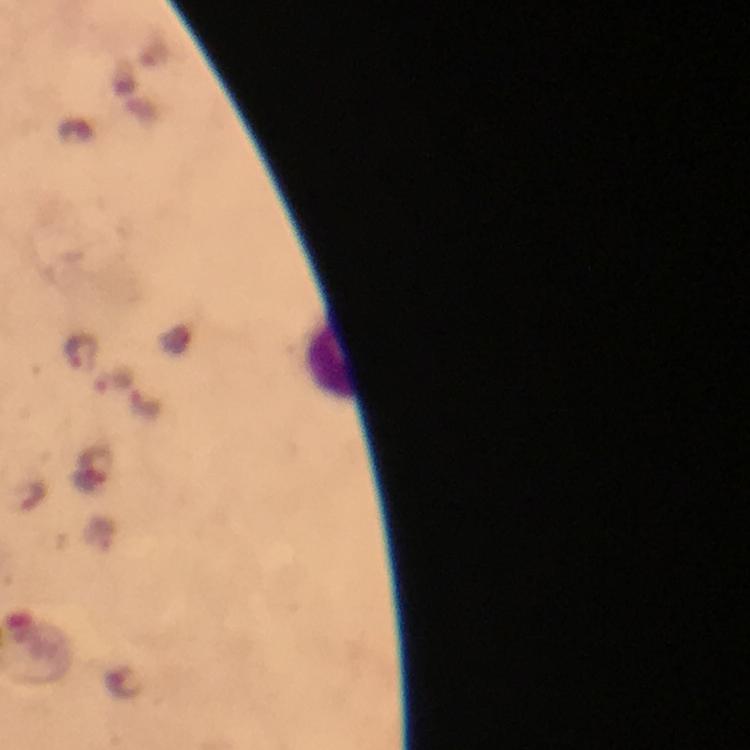

Approximate object centers, in pixels from the top-left corner. Malaria parasite locations: (x=81, y=351), (x=115, y=380). Thick blood film. Photographed through the microscope with a smartphone camera. From a diagnostic examination for malaria. At 100x magnification. Cropped region of a single field of view. Image is 750×750 pixels. Immersion oil applied. Giemsa stain.